Evaluate for malaria.
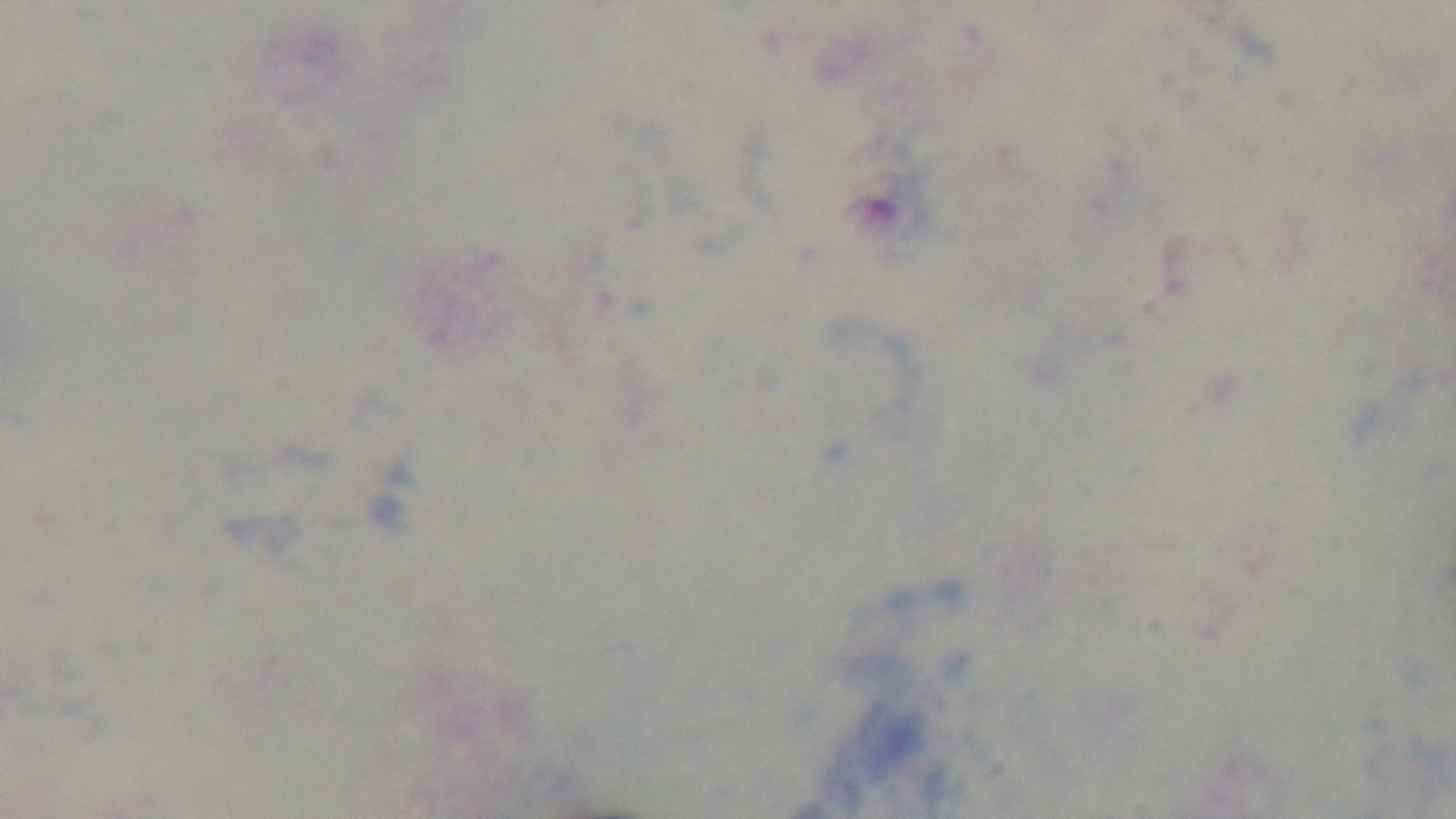
It is uninfected.

Preparation: thick. 100x oil-immersion objective. One field from the slide. Photomicrograph. Giemsa stain. Mounted 4K digital camera.